Assess the morphology of the red blood cells.
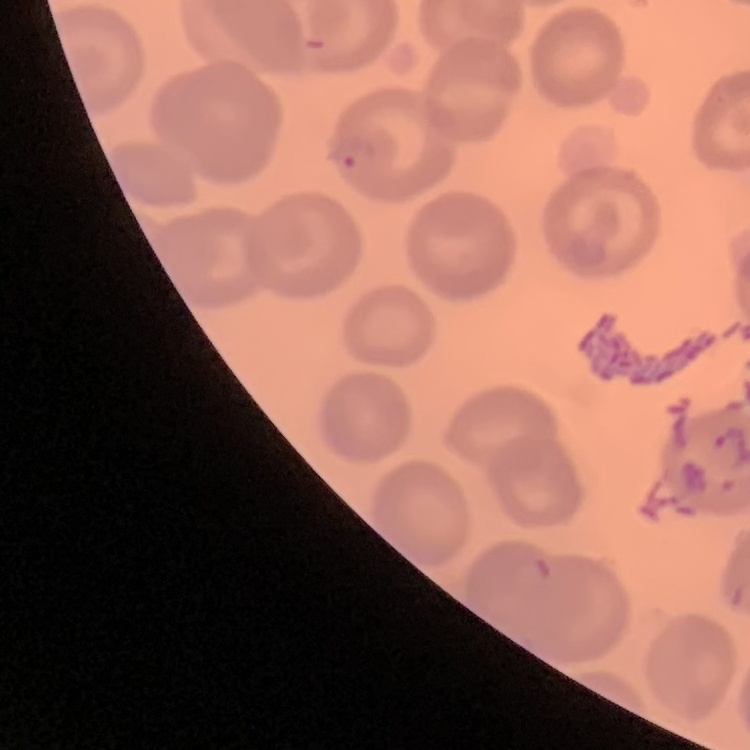

They show no rouleaux formation.

Stained with either Field's or Giemsa. Thin blood smear. One tile cut from a larger photomicrograph.